Identify the parasite.
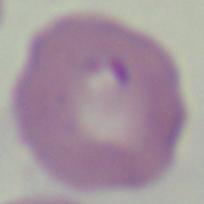
This is Babesia.

Summary:
  - Magnification: 1000x
  - Modality: micrograph